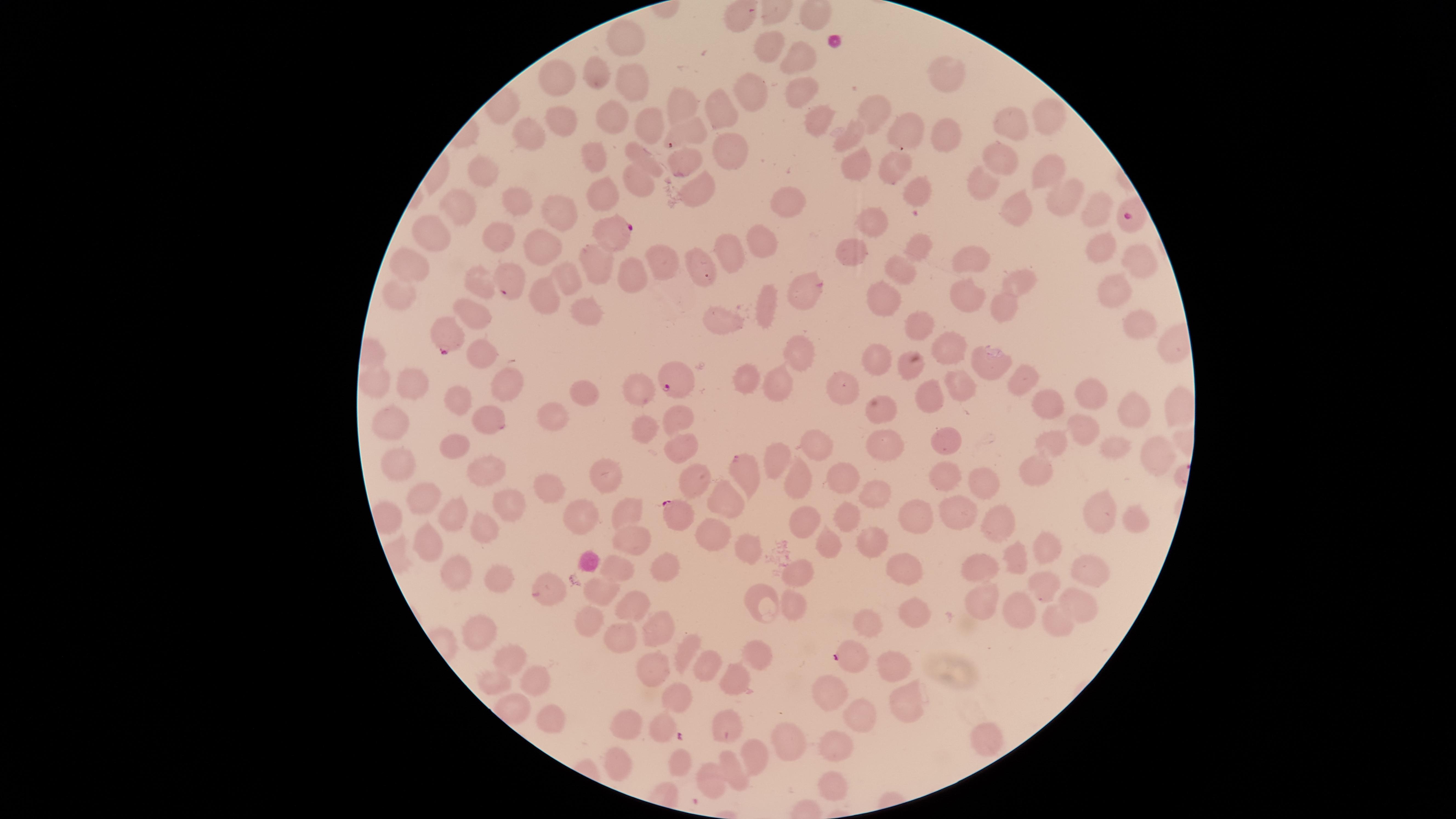

Approximate marker points as [x, y] in pixels.
Summary:
  - Uninfected red blood cells: [735, 18], [623, 37], [765, 51], [793, 63], [945, 71], [594, 73], [555, 81], [627, 86], [749, 89], [794, 93], [678, 100], [721, 106], [875, 108], [608, 117], [1053, 117], [562, 121], [815, 122], [638, 126], [904, 126], [1012, 127], [692, 131], [849, 132], [950, 135], [524, 142], [725, 149], [594, 157], [1000, 158], [644, 159], [685, 162], [854, 167], [485, 170], [895, 170], [1048, 173], [636, 186], [701, 190], [920, 190], [979, 190], [599, 191], [1063, 192], [789, 201], [458, 204], [517, 204], [1010, 206], [1097, 208], [562, 209], [875, 218], [499, 233], [430, 239], [537, 241], [760, 241], [730, 247], [1104, 247], [917, 248], [852, 250], [973, 255], [593, 257], [1136, 257], [661, 263], [696, 264], [413, 268], [634, 272], [899, 273], [564, 276], [476, 280], [1025, 282], [1114, 285], [803, 293], [397, 296], [968, 300], [542, 302], [884, 302], [998, 302], [762, 305], [583, 312], [471, 316], [731, 318], [923, 322], [1145, 325], [949, 351], [480, 352], [798, 352], [875, 357], [991, 361], [906, 368], [1017, 377], [744, 380], [774, 380], [374, 383], [836, 385], [411, 386], [965, 387], [507, 388], [640, 388], [585, 392], [1086, 393], [928, 394], [1049, 402], [460, 404], [1130, 410], [559, 414], [675, 419], [484, 421], [396, 425], [644, 426], [1084, 428], [452, 441], [1049, 445], [883, 446], [947, 446], [1115, 446], [678, 447], [817, 449], [1156, 457], [779, 463], [402, 464], [1033, 468], [746, 472], [489, 473], [607, 474], [696, 474], [947, 476], [981, 479], [793, 480], [840, 482], [546, 485], [870, 492], [725, 494], [518, 503], [419, 504], [958, 509], [1100, 511], [626, 514], [584, 517], [914, 518], [456, 519], [842, 521], [1001, 521], [1131, 522], [802, 525], [484, 527], [710, 528], [867, 538], [430, 542], [824, 543], [745, 546], [627, 550], [1049, 550], [1016, 555], [903, 564], [797, 568], [982, 568], [1089, 568], [456, 570], [616, 571], [666, 571], [498, 581], [1046, 586], [547, 587], [604, 588], [762, 594], [977, 596], [632, 603], [797, 603], [1077, 603], [909, 609], [1017, 609], [1057, 614], [590, 618], [863, 625], [657, 626], [473, 636], [619, 641], [677, 652], [758, 652], [516, 656], [891, 664], [703, 666], [654, 668], [529, 673], [497, 679], [733, 681], [826, 692], [681, 698], [906, 702], [516, 709], [549, 715], [862, 715], [663, 721], [619, 722], [720, 728], [984, 740], [785, 741], [831, 744], [757, 754], [614, 764], [676, 764], [732, 770], [708, 779], [831, 785]
  - Parasitized red blood cells: [1130, 218], [617, 231], [508, 282], [445, 333], [672, 383], [674, 511], [849, 658]
  - Species: Plasmodium falciparum
  - Presence: malaria parasites seen
  - Capture: smartphone photograph through the microscope eyepiece
  - Stain: Giemsa
  - Image size: 1456×819 pixels
  - Preparation: thin blood smear
  - Visible region: circular
  - Field of view: single